Name the parasite shown.
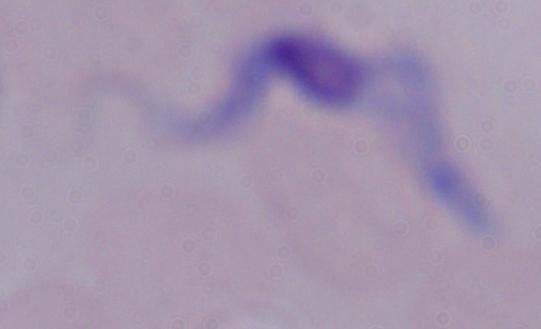
This is a trypanosome.

Micrograph. 1000x magnification.